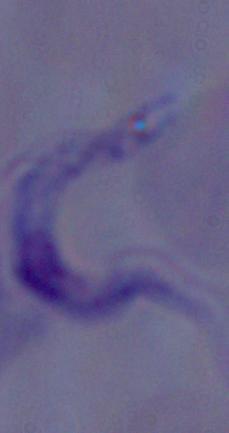 A trypanosome is shown. Micrograph. Captured at 1000x magnification.